Outline each blood parasite and name the species.
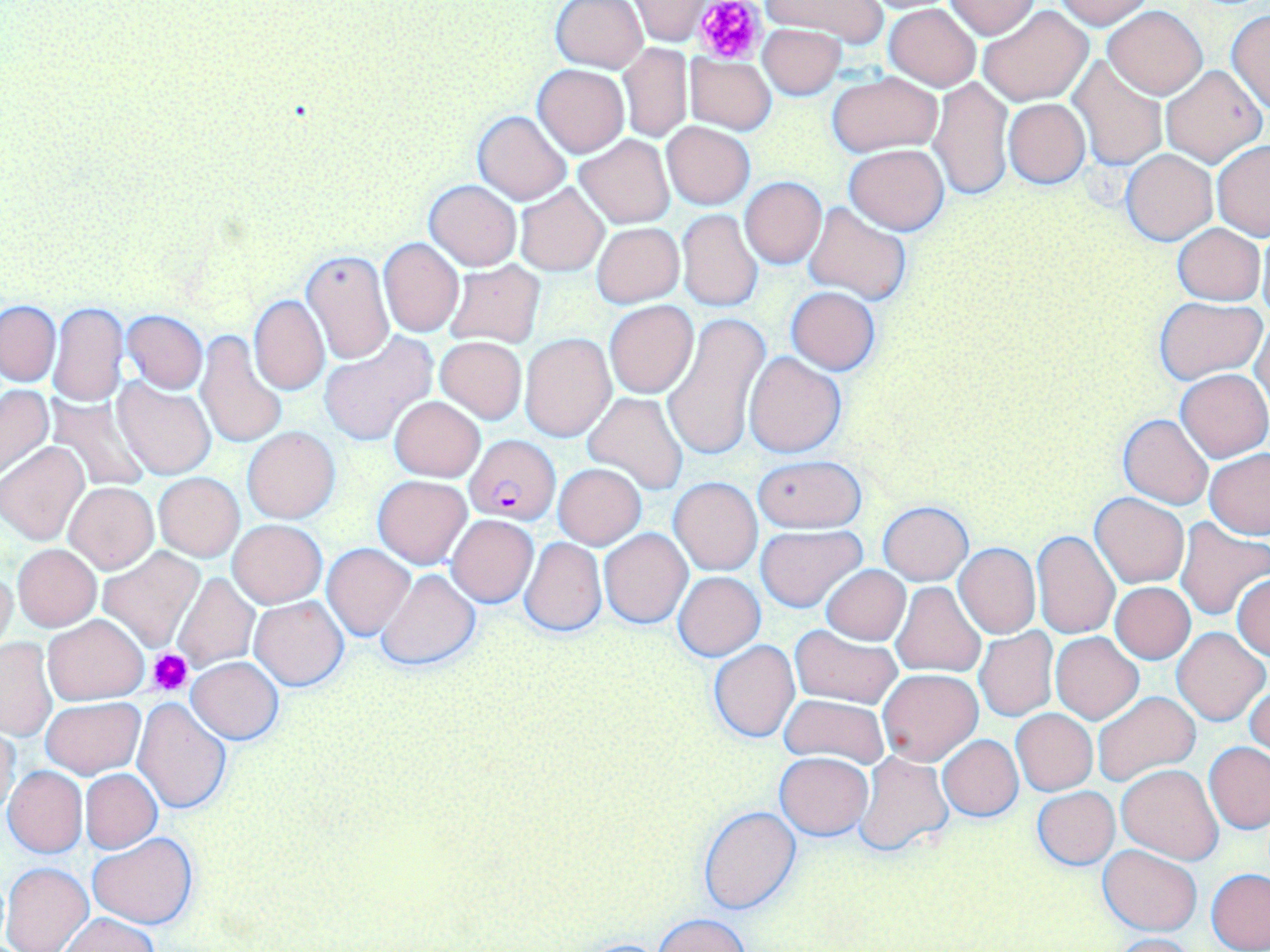

Approximate bounding boxes as named x1/y1/x2/y2 corners in pixels.
Plasmodium falciparum-infected red blood cells: (x1=464, y1=436, x2=561, y2=525).
No Plasmodium ovale, Plasmodium malariae, Plasmodium vivax, Babesia divergens, or Trypanosoma brucei observed.

slide-level diagnosis = Plasmodium falciparum
platelet locations = approximate bounding boxes as named x1/y1/x2/y2 corners in pixels: (x1=694, y1=0, x2=764, y2=61), (x1=147, y1=647, x2=194, y2=696)
uninfected red blood cell locations = approximate bounding boxes as named x1/y1/x2/y2 corners in pixels: (x1=757, y1=0, x2=889, y2=46), (x1=945, y1=0, x2=1039, y2=38), (x1=1051, y1=0, x2=1154, y2=28), (x1=550, y1=1, x2=648, y2=72), (x1=629, y1=1, x2=715, y2=44), (x1=883, y1=3, x2=981, y2=89), (x1=979, y1=5, x2=1093, y2=105), (x1=1104, y1=5, x2=1206, y2=98), (x1=1226, y1=9, x2=1270, y2=113), (x1=758, y1=24, x2=846, y2=97), (x1=620, y1=44, x2=692, y2=141), (x1=686, y1=55, x2=776, y2=134), (x1=1069, y1=56, x2=1166, y2=169), (x1=532, y1=64, x2=629, y2=157), (x1=1161, y1=64, x2=1265, y2=166), (x1=826, y1=72, x2=941, y2=157), (x1=928, y1=75, x2=1012, y2=201), (x1=1003, y1=98, x2=1090, y2=188), (x1=472, y1=111, x2=571, y2=204), (x1=663, y1=122, x2=755, y2=209), (x1=575, y1=134, x2=674, y2=227), (x1=1212, y1=139, x2=1270, y2=239), (x1=844, y1=144, x2=950, y2=233), (x1=1121, y1=149, x2=1217, y2=245), (x1=739, y1=177, x2=826, y2=268), (x1=424, y1=179, x2=521, y2=270), (x1=514, y1=184, x2=608, y2=276), (x1=804, y1=202, x2=911, y2=305), (x1=676, y1=209, x2=761, y2=312), (x1=593, y1=222, x2=684, y2=307), (x1=1172, y1=223, x2=1265, y2=305), (x1=1257, y1=231, x2=1270, y2=325), (x1=379, y1=238, x2=464, y2=335), (x1=300, y1=248, x2=395, y2=366), (x1=444, y1=261, x2=545, y2=347), (x1=269, y1=282, x2=373, y2=390), (x1=785, y1=287, x2=881, y2=374), (x1=249, y1=295, x2=329, y2=396), (x1=1155, y1=297, x2=1265, y2=383), (x1=604, y1=300, x2=698, y2=397), (x1=1, y1=301, x2=60, y2=385), (x1=49, y1=303, x2=128, y2=406), (x1=121, y1=310, x2=208, y2=394), (x1=665, y1=313, x2=771, y2=464), (x1=1251, y1=317, x2=1269, y2=413), (x1=195, y1=329, x2=288, y2=451), (x1=520, y1=332, x2=617, y2=442), (x1=318, y1=335, x2=437, y2=446), (x1=436, y1=337, x2=526, y2=423), (x1=744, y1=351, x2=846, y2=458), (x1=1177, y1=368, x2=1270, y2=462), (x1=113, y1=378, x2=215, y2=479), (x1=0, y1=384, x2=54, y2=480), (x1=584, y1=391, x2=688, y2=494), (x1=45, y1=395, x2=154, y2=493), (x1=389, y1=396, x2=485, y2=481), (x1=1119, y1=413, x2=1215, y2=510), (x1=243, y1=427, x2=340, y2=523), (x1=0, y1=441, x2=89, y2=544), (x1=1204, y1=450, x2=1270, y2=539), (x1=754, y1=457, x2=865, y2=533), (x1=553, y1=463, x2=647, y2=549), (x1=154, y1=472, x2=244, y2=561), (x1=372, y1=475, x2=472, y2=569), (x1=669, y1=477, x2=762, y2=575), (x1=64, y1=481, x2=158, y2=572), (x1=1091, y1=492, x2=1189, y2=588), (x1=879, y1=501, x2=972, y2=585), (x1=619, y1=506, x2=723, y2=614), (x1=446, y1=514, x2=539, y2=607), (x1=229, y1=519, x2=326, y2=608), (x1=1174, y1=519, x2=1270, y2=619), (x1=755, y1=525, x2=867, y2=613), (x1=599, y1=527, x2=692, y2=628), (x1=1032, y1=531, x2=1120, y2=639), (x1=519, y1=536, x2=607, y2=636), (x1=322, y1=543, x2=414, y2=640), (x1=954, y1=544, x2=1039, y2=638), (x1=13, y1=545, x2=101, y2=630), (x1=96, y1=548, x2=205, y2=651), (x1=0, y1=565, x2=17, y2=658), (x1=822, y1=565, x2=910, y2=644), (x1=377, y1=569, x2=481, y2=672), (x1=673, y1=572, x2=765, y2=660), (x1=172, y1=573, x2=260, y2=671), (x1=1232, y1=574, x2=1270, y2=661), (x1=891, y1=582, x2=985, y2=677), (x1=1111, y1=582, x2=1196, y2=663), (x1=250, y1=596, x2=348, y2=691), (x1=43, y1=614, x2=149, y2=705), (x1=790, y1=625, x2=901, y2=707), (x1=1171, y1=627, x2=1267, y2=725), (x1=973, y1=628, x2=1058, y2=722), (x1=1051, y1=632, x2=1143, y2=723), (x1=1, y1=637, x2=57, y2=741), (x1=707, y1=640, x2=800, y2=742), (x1=187, y1=657, x2=283, y2=743), (x1=878, y1=669, x2=982, y2=765), (x1=1245, y1=672, x2=1269, y2=765), (x1=1093, y1=691, x2=1201, y2=790), (x1=778, y1=694, x2=890, y2=769), (x1=41, y1=697, x2=144, y2=779), (x1=133, y1=697, x2=232, y2=812), (x1=1012, y1=709, x2=1096, y2=795), (x1=1, y1=725, x2=21, y2=823), (x1=938, y1=735, x2=1022, y2=821), (x1=1204, y1=742, x2=1270, y2=833), (x1=855, y1=752, x2=953, y2=857), (x1=775, y1=753, x2=874, y2=839), (x1=1117, y1=763, x2=1223, y2=863), (x1=3, y1=765, x2=87, y2=857), (x1=81, y1=769, x2=161, y2=852), (x1=1032, y1=787, x2=1120, y2=869), (x1=699, y1=806, x2=802, y2=914), (x1=89, y1=832, x2=196, y2=930), (x1=1097, y1=846, x2=1203, y2=935), (x1=2, y1=862, x2=94, y2=952), (x1=1205, y1=869, x2=1270, y2=951), (x1=60, y1=912, x2=160, y2=952), (x1=653, y1=914, x2=754, y2=952), (x1=1104, y1=933, x2=1200, y2=952)
field of view = single
magnification = 1000x
stain = May-Grünwald-Giemsa
image size = 1270×952 pixels
modality = light microscopy
preparation = thin blood smear